Identify the blood parasite species.
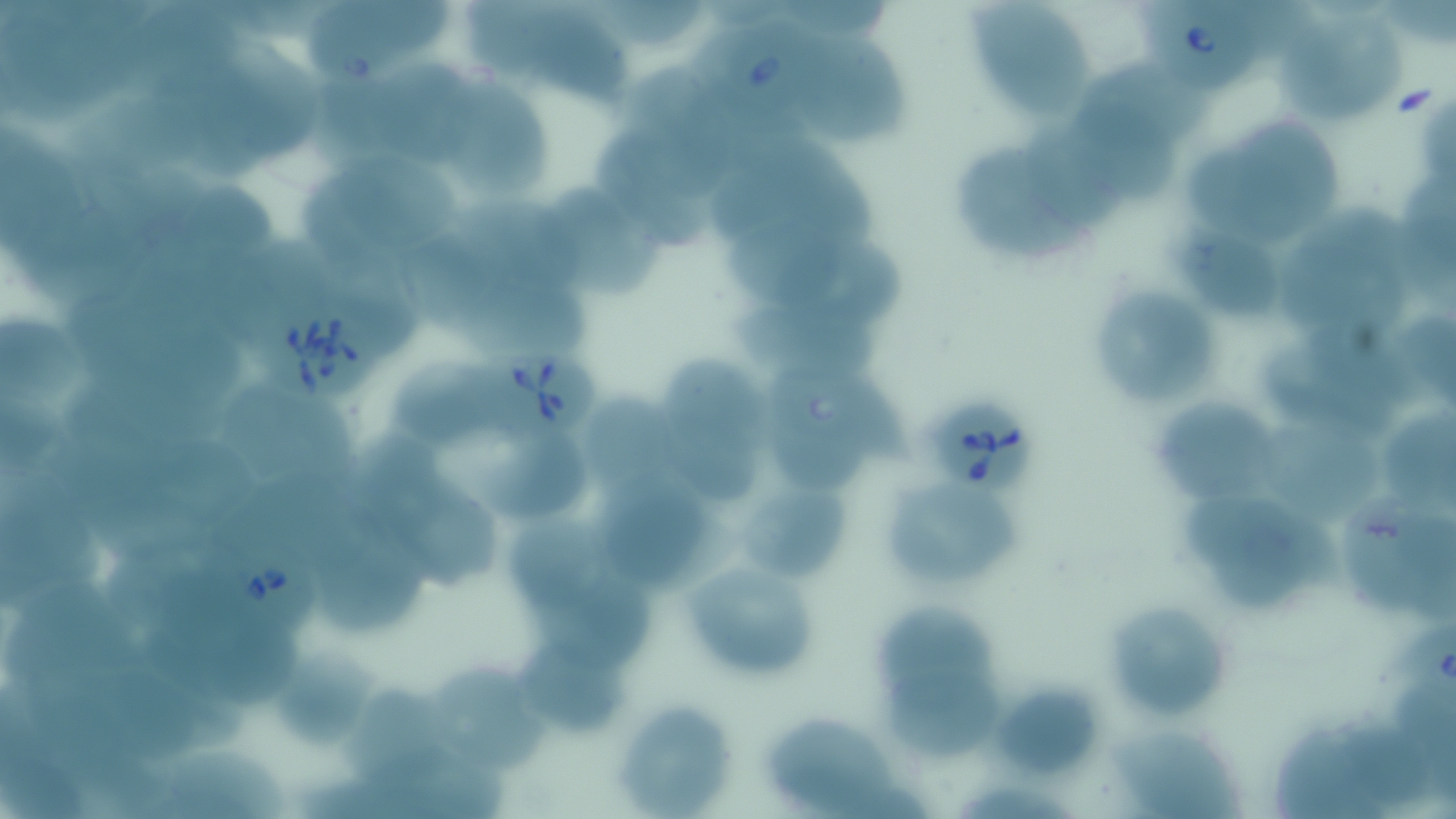

Babesia divergens.

Approximate bounding boxes as (x1, y1, x2, y2) in pixels. Babesia divergens-infected red blood cell locations: (1133, 1, 1271, 96), (699, 8, 835, 131), (245, 298, 384, 398), (475, 350, 603, 441), (767, 363, 915, 463), (929, 394, 1041, 494), (201, 535, 326, 641), (1391, 621, 1456, 703). Uninfected red blood cell locations: (305, 0, 452, 82), (966, 0, 1095, 127), (99, 9, 249, 101), (507, 10, 633, 99), (1277, 18, 1405, 126), (802, 35, 917, 148), (211, 40, 326, 162), (376, 60, 488, 164), (624, 61, 737, 195), (1081, 62, 1213, 145), (433, 79, 553, 201), (1070, 101, 1182, 204), (1224, 108, 1352, 242), (0, 122, 99, 259), (595, 123, 718, 246), (1029, 128, 1121, 223), (782, 135, 884, 243), (954, 141, 1102, 261), (313, 143, 463, 257), (1407, 167, 1456, 263), (547, 175, 658, 299), (189, 181, 278, 262), (451, 193, 587, 301), (1301, 201, 1432, 292), (1163, 209, 1289, 320), (724, 216, 859, 307), (813, 229, 909, 328), (404, 234, 494, 333), (1269, 243, 1410, 331), (1101, 283, 1213, 404), (468, 285, 593, 357), (717, 294, 886, 391), (1404, 311, 1456, 401), (1303, 314, 1421, 399), (1, 315, 83, 404), (1265, 346, 1391, 439), (651, 352, 777, 450), (397, 356, 494, 439), (227, 386, 363, 486), (1158, 392, 1294, 508), (586, 396, 683, 482), (0, 401, 68, 475), (1387, 409, 1456, 510), (1263, 414, 1391, 534), (770, 421, 876, 486), (667, 430, 760, 502), (353, 431, 459, 542), (156, 439, 260, 528), (491, 439, 594, 521), (225, 466, 388, 559), (875, 470, 1030, 593), (739, 476, 849, 586), (603, 479, 738, 585), (408, 481, 506, 594), (1339, 496, 1432, 608), (0, 497, 105, 590), (1183, 500, 1316, 590), (502, 508, 622, 615), (324, 546, 431, 634), (677, 558, 823, 679), (535, 563, 661, 683), (22, 577, 137, 680), (1100, 597, 1234, 724), (864, 603, 1004, 711), (216, 625, 313, 705), (520, 642, 636, 732), (268, 645, 380, 749), (881, 660, 1010, 763), (426, 661, 567, 774), (76, 664, 201, 762), (988, 678, 1107, 782), (336, 680, 458, 784), (613, 697, 740, 816), (755, 710, 913, 816), (1275, 721, 1389, 819), (1342, 724, 1435, 808), (1104, 726, 1244, 816), (168, 748, 295, 819), (0, 755, 80, 819). Thin blood film. Single field of view. Light microscopy. May-Grünwald-Giemsa stain. Image is 1456×819 pixels. 1000x magnification.